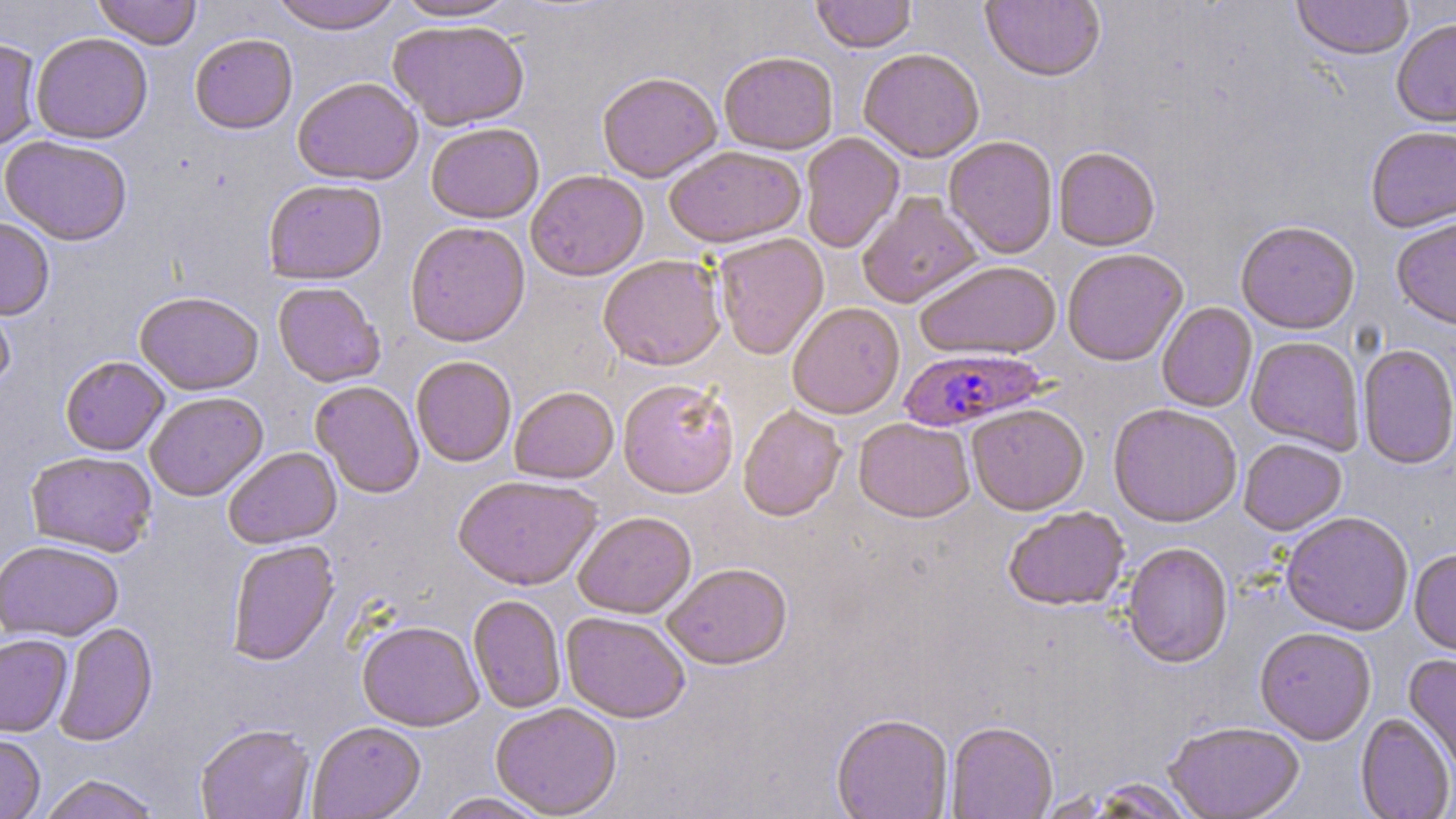
slide_level_diagnosis: Plasmodium falciparum
stain: May-Grünwald-Giemsa
preparation: thin blood smear
uninfected_red_blood_cell_locations: 'approximate bounding boxes as (x1, y1, x2, y2) in pixels: (93, 0, 201, 49), (267, 0, 405, 34), (393, 0, 518, 22), (811, 0, 917, 53), (1292, 0, 1414, 62), (980, 1, 1105, 84), (388, 19, 530, 131), (1392, 19, 1456, 128), (31, 31, 152, 143), (189, 33, 298, 134), (0, 37, 42, 152), (858, 49, 984, 162), (719, 50, 838, 154), (597, 71, 721, 183), (292, 76, 424, 186), (425, 122, 544, 223), (1365, 126, 1456, 233), (800, 133, 904, 254), (0, 135, 133, 245), (943, 136, 1058, 259), (663, 144, 806, 249), (1054, 147, 1160, 251), (526, 169, 649, 281), (263, 179, 387, 285), (856, 192, 982, 308), (0, 217, 55, 319), (1391, 219, 1456, 331), (405, 221, 530, 347), (1236, 221, 1360, 335), (713, 233, 829, 360), (1062, 249, 1188, 367), (597, 254, 726, 371), (915, 261, 1062, 360), (273, 281, 385, 387), (0, 285, 16, 397), (134, 291, 263, 396), (788, 303, 905, 419), (1156, 303, 1257, 413), (1246, 336, 1364, 454), (1357, 344, 1456, 470), (60, 355, 170, 456), (410, 356, 517, 467), (617, 378, 740, 498), (310, 380, 425, 499), (509, 386, 619, 483), (144, 391, 269, 501), (966, 404, 1089, 516), (1107, 404, 1242, 528), (738, 405, 848, 522), (854, 418, 975, 523), (1238, 439, 1347, 536), (223, 447, 341, 549), (25, 450, 157, 556), (453, 475, 602, 591), (1004, 506, 1129, 611), (573, 511, 696, 619), (1281, 513, 1413, 635), (0, 539, 123, 642), (226, 540, 339, 666), (1121, 543, 1234, 669), (1409, 550, 1456, 658), (662, 563, 792, 670), (468, 595, 566, 713), (561, 612, 690, 723), (357, 620, 483, 731), (54, 622, 158, 747), (1254, 628, 1376, 745), (0, 634, 73, 737), (1403, 655, 1456, 776), (490, 703, 622, 817), (831, 714, 953, 819), (1355, 714, 1455, 819), (307, 721, 426, 819), (195, 723, 315, 819), (946, 723, 1058, 819), (1164, 723, 1305, 819), (0, 733, 46, 819), (38, 774, 162, 819), (1087, 778, 1196, 818), (434, 792, 550, 819)'
plasmodium_falciparum_infected_red_blood_cell_locations: 'approximate bounding boxes as (x1, y1, x2, y2) in pixels: (899, 347, 1048, 432)'
field_of_view: one of a larger specimen
magnification: 1000x
modality: optical microscopy
image_size: 1456×819 pixels